Assess this cell for malaria.
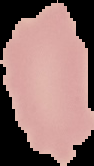
It is uninfected.

From a thin blood smear. Cell region segmented out of the field of view; the surrounding area is masked to black. Image is 94×166 pixels.